Report the malaria status of this cell.
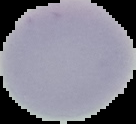

It is uninfected.

Summary:
  - Image type: segmented cell region on a black background
  - Image size: 136×124 pixels
  - Preparation: thin blood film